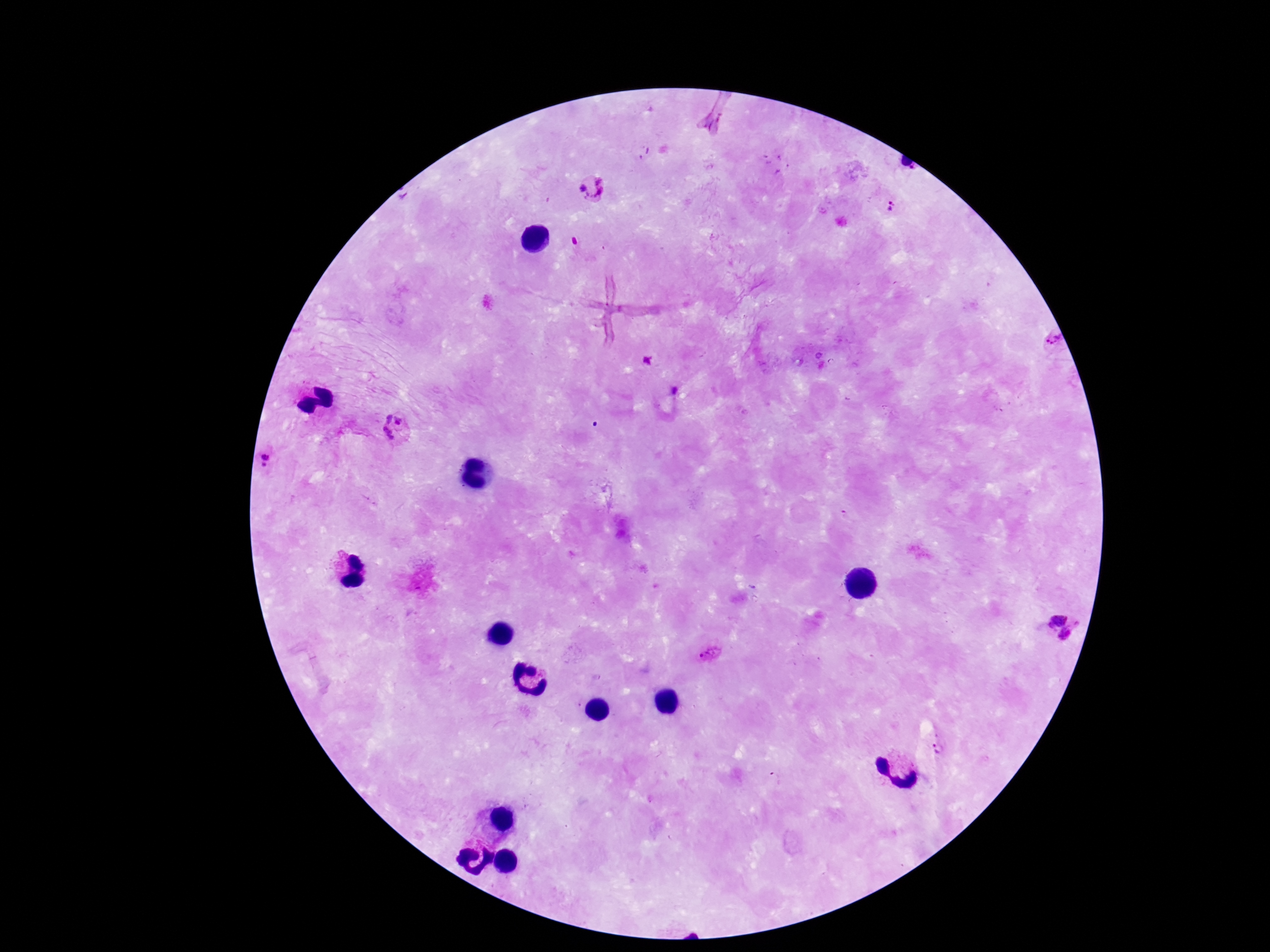 Approximate centers as {x, y} in pixels. Plasmodium parasite locations: {593, 189}, {890, 205}, {1048, 343}, {647, 361}, {676, 391}, {394, 430}, {271, 461}, {1055, 615}, {1065, 636}, {710, 655}, {938, 748}. 100x magnification. Image is 1270×952 pixels. Patient malaria status: positive. Single field of view. Smartphone photograph taken through the microscope eyepiece. Giemsa-stained preparation. Thick blood film.